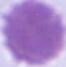

An erythrocyte is seen. Micrograph. Captured at 1000x magnification.